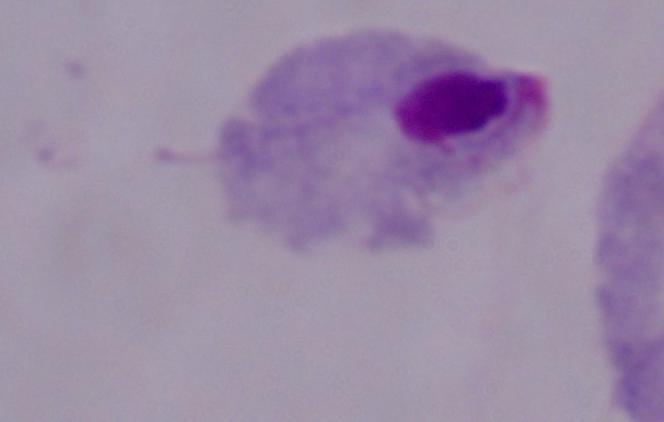
identification = trichomonad
magnification = 1000x
modality = micrograph